Give the position of every Plasmodium parasite.
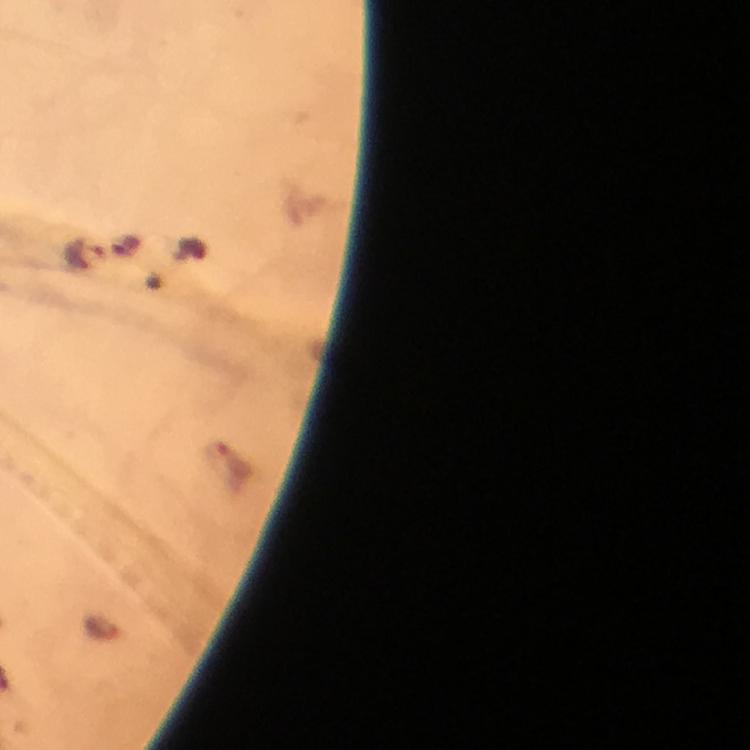

Approximate object centers, in pixels from the top-left corner.
Plasmodium parasites: (x=84, y=254).

immersion oil = used
preparation = thick blood film
stain = Giemsa
capture = smartphone photograph through a microscope
cropped from = a single field of view
context = from a diagnostic examination for malaria
image size = 750×750 pixels
magnification = 100x